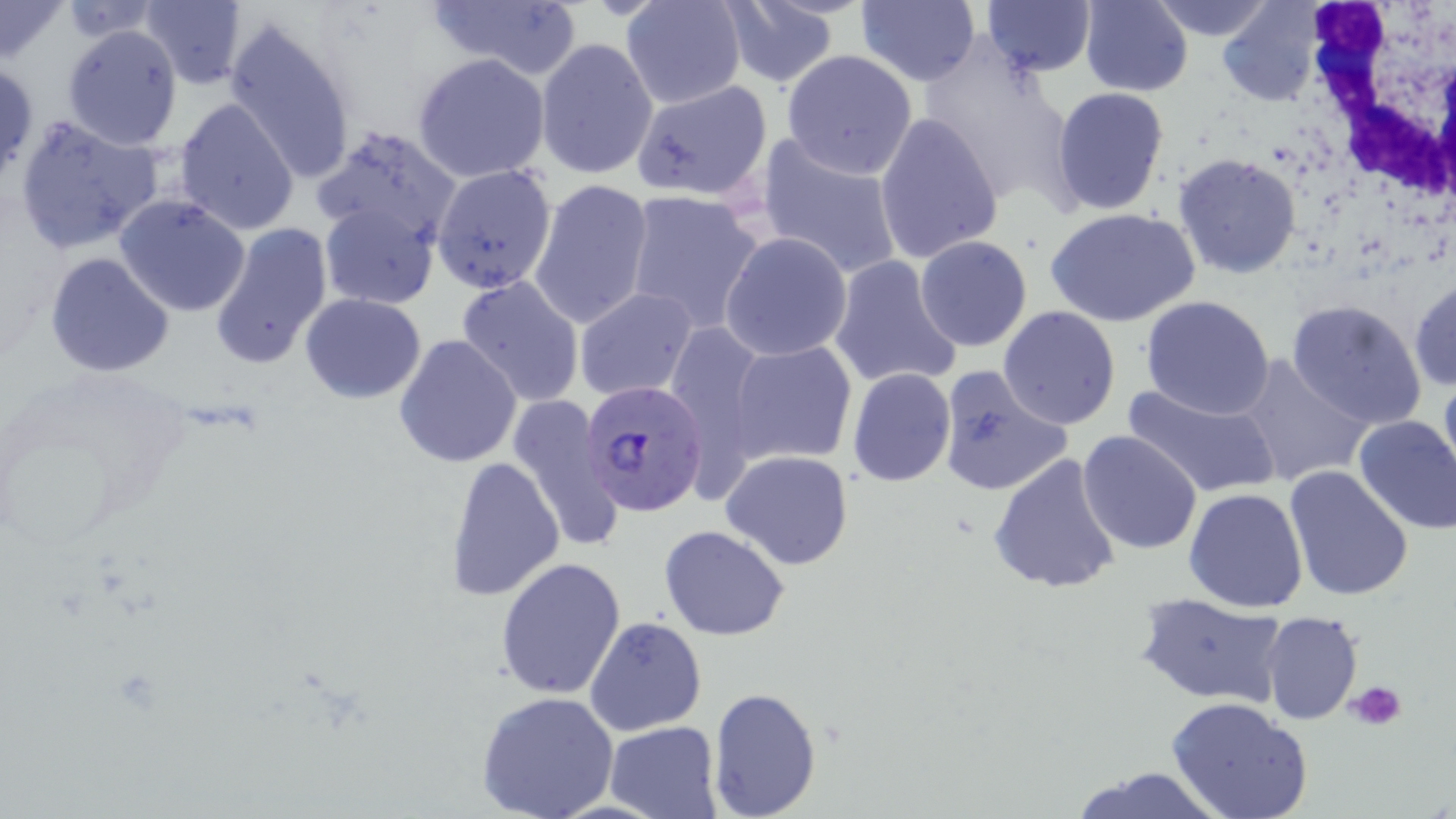

slide-level diagnosis = Plasmodium falciparum
magnification = 1000x
modality = light microscopy
preparation = thin blood smear
field of view = single
stain = May-Grünwald-Giemsa
uninfected red blood cell locations = approximate bounding boxes as (x1,y1)-(x2,y2) corner pairs in pixels: (139,0)-(248,88), (426,0)-(582,80), (621,0)-(747,109), (855,0)-(982,87), (978,1)-(1098,78), (1080,1)-(1195,96), (1149,1)-(1278,43), (1216,1)-(1326,107), (0,2)-(68,64), (60,2)-(167,43), (715,2)-(843,90), (222,15)-(360,186), (61,23)-(183,149), (534,37)-(657,181), (920,44)-(1075,203), (779,50)-(919,177), (412,52)-(550,184), (631,69)-(767,203), (1050,85)-(1171,215), (174,97)-(301,236), (874,112)-(1004,264), (14,114)-(163,254), (314,128)-(462,250), (755,133)-(905,283), (1173,153)-(1302,279), (431,162)-(558,294), (529,177)-(654,332), (624,189)-(767,332), (114,195)-(253,318), (320,201)-(439,310), (1044,206)-(1200,329), (209,222)-(334,370), (720,232)-(854,361), (914,236)-(1032,352), (44,252)-(175,378), (829,255)-(965,391), (455,275)-(585,406), (1408,277)-(1456,392), (574,288)-(699,402), (299,294)-(427,405), (1140,296)-(1275,421), (1285,299)-(1428,430), (998,306)-(1122,430), (394,333)-(523,469), (726,338)-(857,468), (1233,354)-(1371,486), (935,365)-(1073,499), (847,367)-(957,485), (1438,369)-(1456,491), (1123,378)-(1281,500), (510,393)-(624,557), (1352,414)-(1456,534), (1077,430)-(1202,554), (720,450)-(856,570), (988,453)-(1123,596), (442,457)-(565,601), (1283,465)-(1415,603), (1184,487)-(1309,612), (659,526)-(791,641), (495,557)-(627,702), (1135,593)-(1287,707), (1261,611)-(1364,726), (585,616)-(706,735), (706,685)-(823,818), (475,691)-(618,819), (1166,697)-(1314,819), (603,721)-(724,818), (1064,764)-(1231,819)
platelet locations = approximate bounding boxes as (x1,y1)-(x2,y2) corner pairs in pixels: (1346,679)-(1408,732)
white blood cell locations = approximate bounding boxes as (x1,y1)-(x2,y2) corner pairs in pixels: (1300,1)-(1455,216)
Plasmodium falciparum-infected red blood cell locations = approximate bounding boxes as (x1,y1)-(x2,y2) corner pairs in pixels: (582,381)-(709,517)
image size = 1456×819 pixels